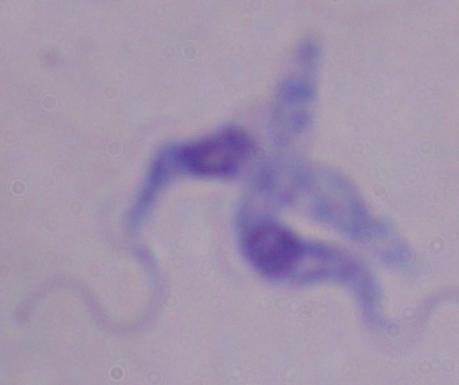

Summary:
  - Identification: trypanosome
  - Magnification: 1000x
  - Modality: photomicrograph